Classify this cell by malaria status.
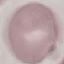

Uninfected.

Summary:
  - Stain: Giemsa
  - Capture: smartphone through the microscope eyepiece
  - Image type: automatically extracted cell patch, resized to 64 × 64 pixels
  - Preparation: thin blood film